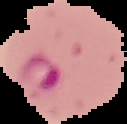 Malaria status: parasitized. The area outside the segmented cell region is set to black. Image is 127×124 pixels. From a thin blood film.